Locate and identify every blood parasite.
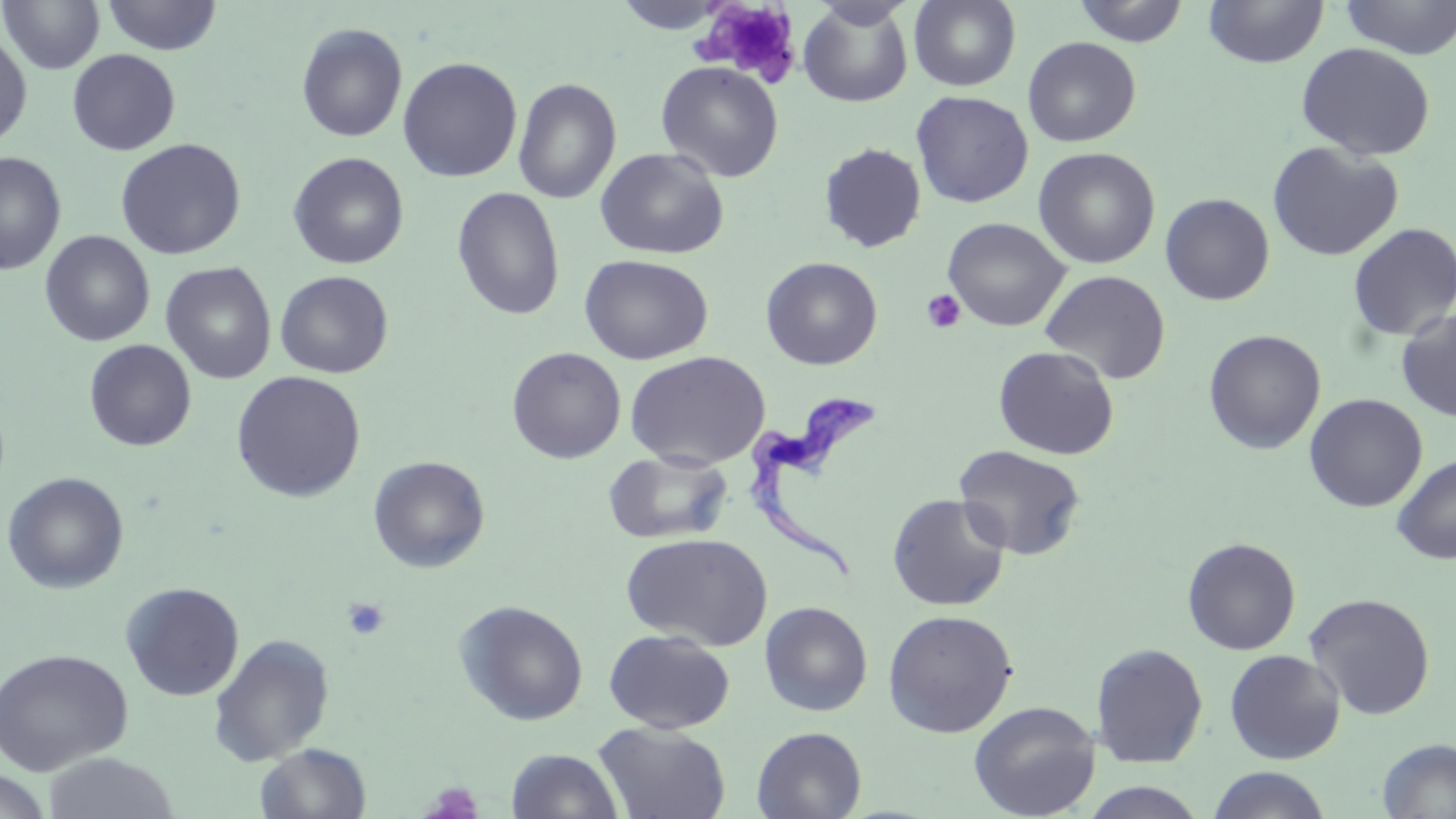

Approximate bounding boxes as (x1,y1)-(x2,y2) corner pairs in pixels.
Trypanosoma brucei: (746,391)-(878,586).
No Plasmodium falciparum, Plasmodium ovale, Plasmodium malariae, Plasmodium vivax, or Babesia divergens observed.

Uninfected red blood cell locations: (0,0)-(104,75), (0,0)-(221,68), (102,0)-(223,56), (612,0)-(731,33), (909,0)-(1021,92), (1072,0)-(1191,47), (1338,0)-(1456,59), (798,1)-(914,108), (1202,1)-(1329,69), (296,22)-(407,142), (0,31)-(32,148), (1022,36)-(1141,147), (1295,42)-(1436,161), (67,49)-(180,156), (398,56)-(522,182), (656,61)-(784,182), (513,77)-(622,204), (910,90)-(1033,208), (115,138)-(246,260), (1266,141)-(1404,262), (819,143)-(927,252), (595,147)-(728,260), (1033,147)-(1160,268), (0,151)-(66,275), (288,151)-(409,269), (451,187)-(565,321), (1160,193)-(1275,305), (942,216)-(1070,331), (1347,222)-(1456,341), (40,230)-(155,347), (579,254)-(714,365), (761,256)-(882,370), (160,262)-(276,384), (1040,269)-(1171,384), (275,271)-(394,378), (1396,309)-(1456,422), (1203,329)-(1326,454), (84,339)-(197,451), (993,345)-(1119,460), (506,346)-(627,464), (625,351)-(770,469), (230,371)-(366,502), (1304,393)-(1428,513), (953,444)-(1086,561), (603,450)-(733,545), (1392,453)-(1456,565), (368,455)-(490,573), (2,471)-(129,593), (887,493)-(1011,611), (621,532)-(772,651), (1182,537)-(1301,655), (120,581)-(244,701), (1304,592)-(1436,719), (454,599)-(589,726), (759,600)-(873,716), (882,608)-(1018,738), (604,629)-(736,734), (208,634)-(334,766), (1090,642)-(1209,768), (0,648)-(133,775), (1225,649)-(1345,764), (969,700)-(1100,818), (593,722)-(731,819), (752,726)-(867,819), (1377,737)-(1456,818), (255,743)-(371,819), (506,748)-(624,818), (41,752)-(181,819), (1206,766)-(1332,819), (0,770)-(53,819), (1078,782)-(1209,818). Platelet locations: (696,3)-(801,84), (921,289)-(966,333), (342,597)-(390,641), (421,782)-(484,819). Slide-level diagnosis: Trypanosoma brucei. Light microscopy. One field of a larger specimen. Thin blood smear. May-Grünwald-Giemsa-stained preparation. Captured at 1000x magnification. Image is 1456×819 pixels.